Assess the morphology of the erythrocytes.
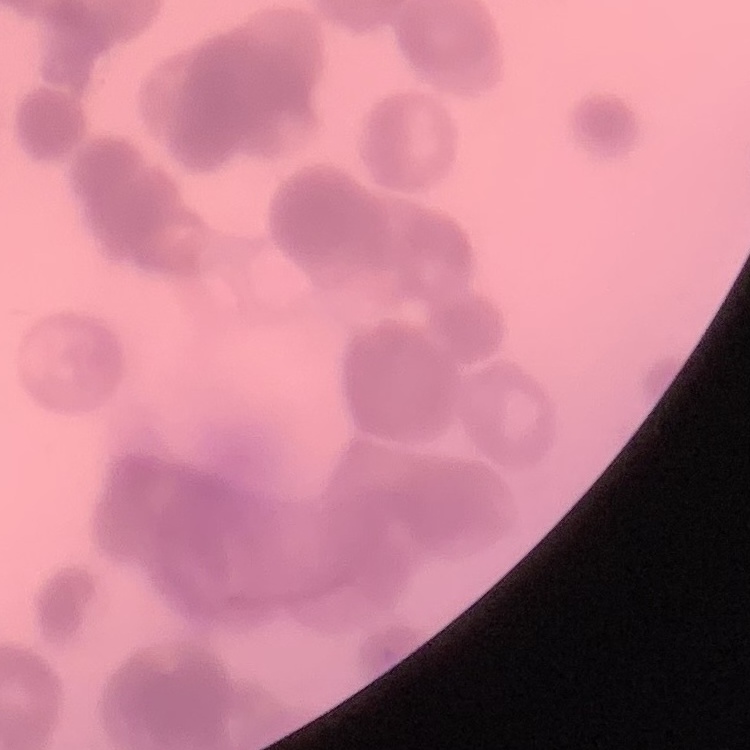
Rouleaux formation.

Stained with either Field's or Giemsa. One tile cut from a larger photomicrograph. Thin peripheral smear.